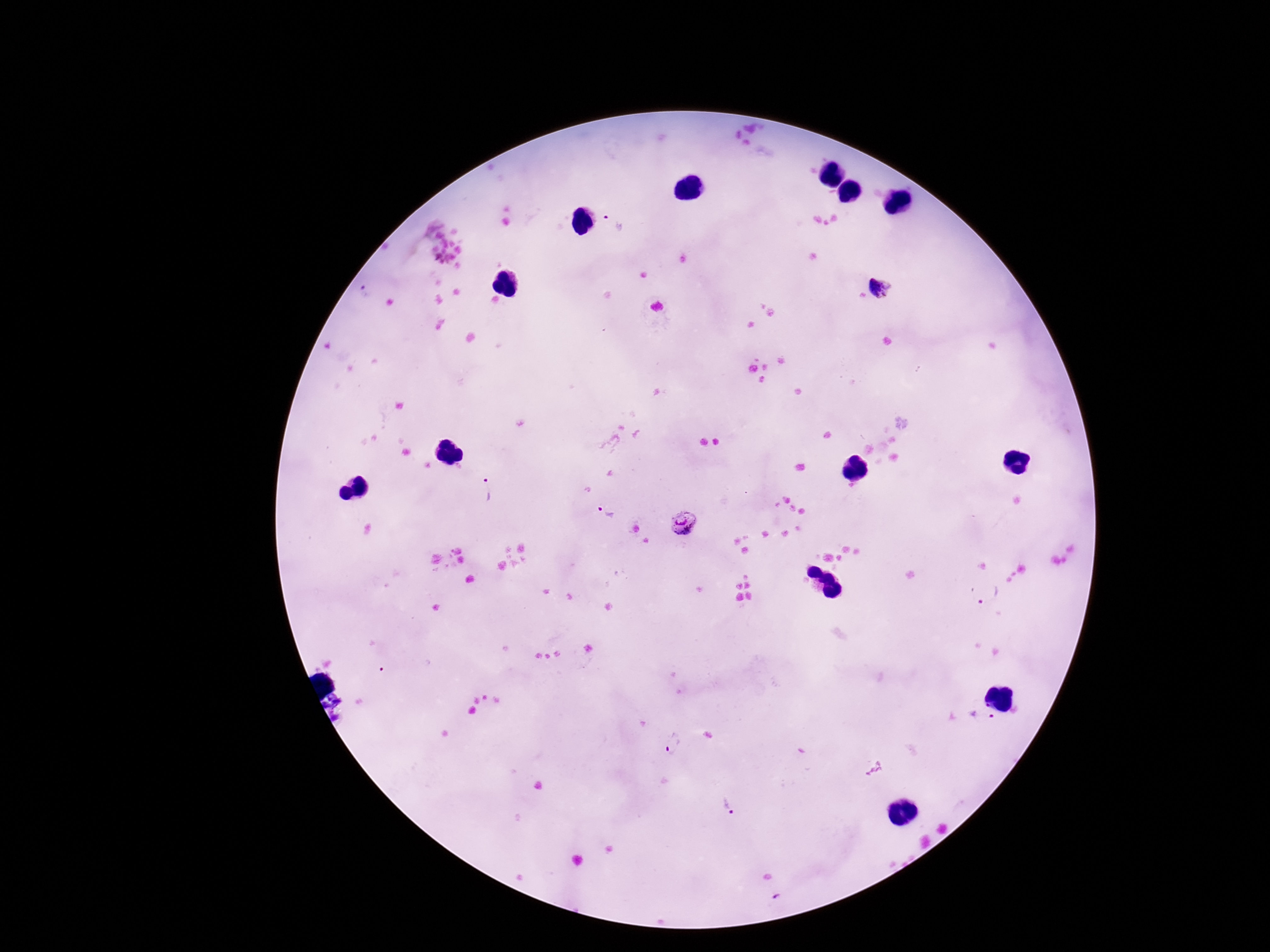

Approximate object centers, in pixels from the top-left corner. Plasmodium parasite locations: (x=612, y=221), (x=883, y=286), (x=367, y=292), (x=486, y=490), (x=606, y=511), (x=682, y=521), (x=988, y=592), (x=981, y=716), (x=674, y=743), (x=727, y=806). 100x magnification. Giemsa stain. Thick peripheral-blood smear. Image is 1270×952 pixels. Patient malaria status: positive. Photographed through the microscope eyepiece with a smartphone camera. Single field of view.